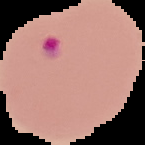

malaria status = parasitized
image type = segmented cell region on a black background
image size = 145×145 pixels
preparation = thin blood smear